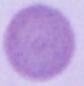

1000x magnification. Photomicrograph. An erythrocyte is shown.